State which parasite is depicted.
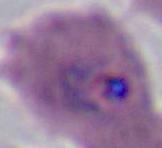
Plasmodium.

Summary:
  - Modality: micrograph
  - Magnification: 400x or 1000x